Name the parasite shown.
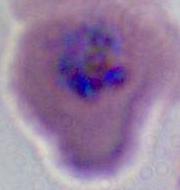
This is Plasmodium.

Summary:
  - Modality: micrograph
  - Magnification: 400x or 1000x